Locate every Plasmodium parasite and every leukocyte.
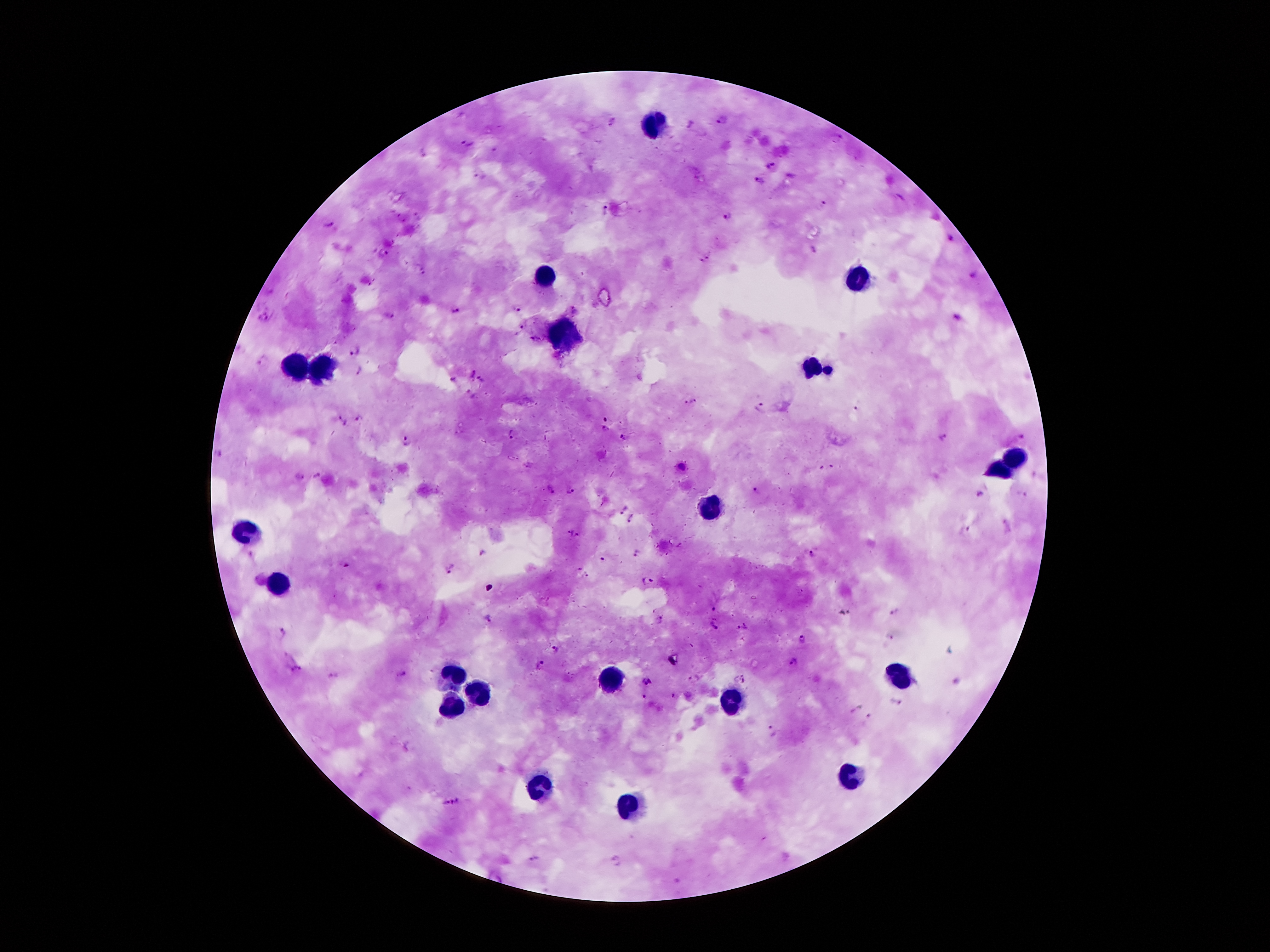

Approximate centers as {x, y} in pixels.
Plasmodium parasites: {722, 119}, {611, 121}, {688, 125}, {467, 143}, {769, 166}, {789, 174}, {480, 177}, {760, 179}, {822, 203}, {605, 210}, {729, 218}, {328, 225}, {948, 240}, {381, 252}, {709, 253}, {700, 262}, {972, 277}, {515, 307}, {453, 310}, {264, 315}, {387, 316}, {959, 320}, {521, 329}, {355, 348}, {261, 361}, {359, 370}, {470, 371}, {482, 378}, {453, 381}, {471, 396}, {691, 403}, {760, 408}, {854, 409}, {606, 417}, {341, 420}, {362, 420}, {604, 428}, {514, 435}, {1021, 436}, {946, 437}, {625, 439}, {409, 442}, {681, 467}, {320, 476}, {297, 478}, {549, 492}, {570, 492}, {760, 492}, {978, 496}, {623, 510}, {632, 520}, {965, 530}, {568, 532}, {577, 536}, {483, 552}, {633, 552}, {813, 554}, {601, 559}, {449, 571}, {577, 571}, {586, 577}, {648, 581}, {714, 609}, {895, 611}, {487, 621}, {657, 621}, {712, 626}, {743, 627}, {281, 632}, {890, 638}, {802, 639}, {558, 648}, {793, 664}, {540, 665}, {297, 670}, {401, 674}, {740, 679}, {646, 680}, {673, 696}, {644, 697}, {899, 702}, {856, 709}, {774, 732}, {451, 803}, {533, 860}, {617, 861}.
Leukocytes: {657, 126}, {543, 278}, {858, 280}, {559, 338}, {811, 364}, {296, 368}, {324, 368}, {829, 370}, {1019, 459}, {998, 469}, {709, 504}, {247, 532}, {282, 583}, {452, 676}, {608, 679}, {895, 679}, {475, 695}, {730, 704}, {452, 707}, {853, 779}, {536, 788}, {627, 807}.

capture = smartphone through the microscope eyepiece
patient malaria status = positive for Plasmodium falciparum
stain = Giemsa
magnification = 100x
image size = 1270×952 pixels
field of view = single
preparation = thick peripheral-blood smear